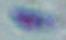

Summary:
  - Identification: Toxoplasma gondii
  - Modality: micrograph
  - Magnification: 1000x